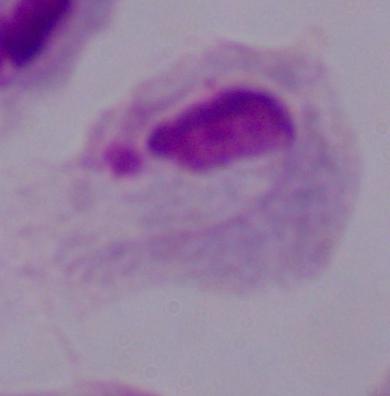
Summary:
  - Modality: photomicrograph
  - Identification: trichomonad
  - Magnification: 1000x